Report the malaria status of this cell.
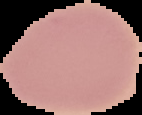

Uninfected.

Summary:
  - Image type: segmented cell region with the area outside set to black
  - Image size: 142×115 pixels
  - Preparation: thin blood smear